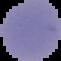
image_size: 61×61 pixels
preparation: thin blood film
image_type: cell region segmented out of the field of view; surrounding area masked to black
malaria_status: parasitized